Locate every blood parasite and identify its species.
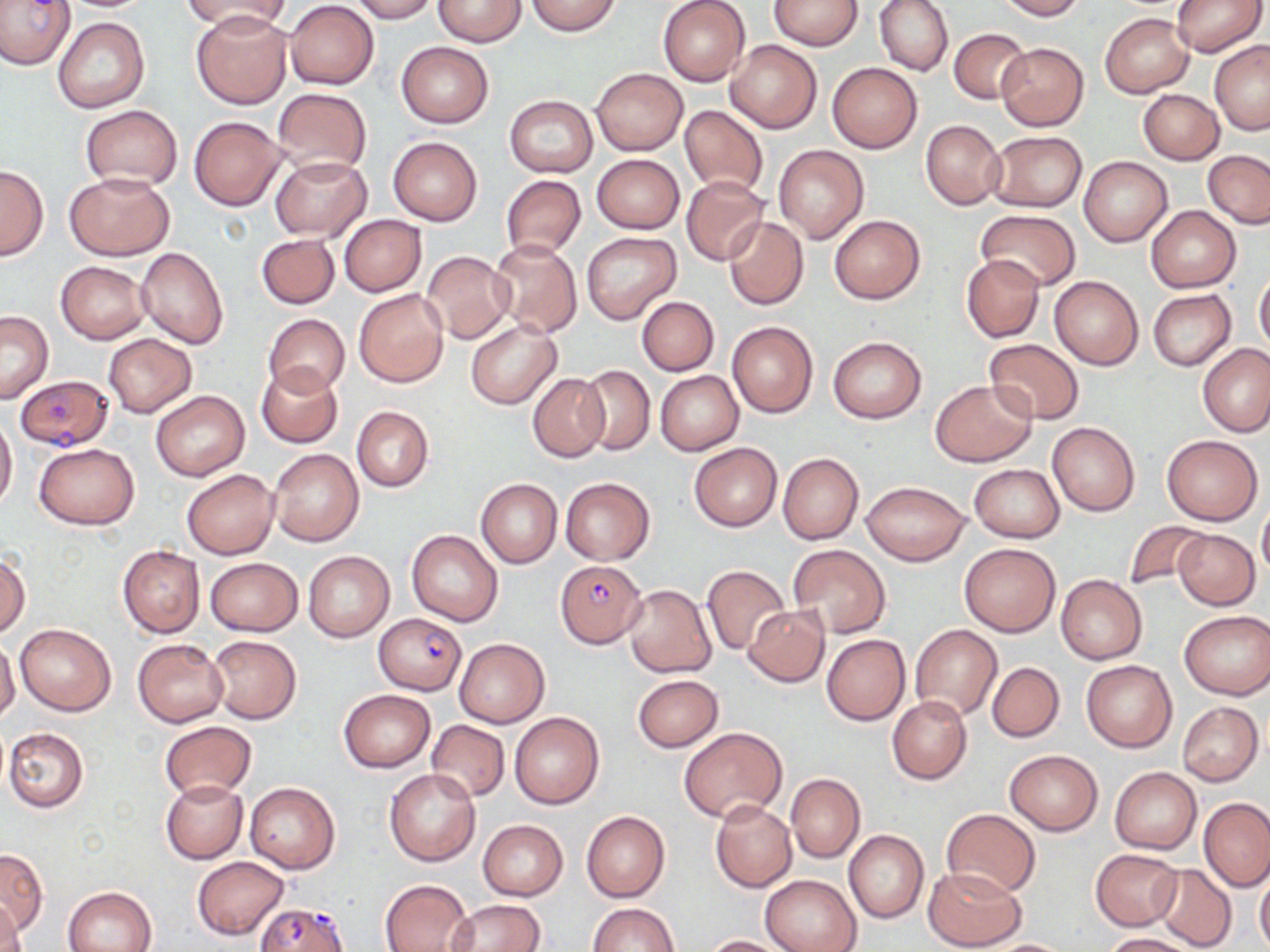
Approximate bounding boxes as [x1, y1, x2, y2] in pixels.
Plasmodium falciparum-infected red blood cells: [0, 0, 75, 69], [14, 375, 113, 450], [555, 559, 647, 647], [373, 612, 468, 694], [254, 902, 349, 952].
No Plasmodium ovale, Plasmodium malariae, Plasmodium vivax, Babesia divergens, or Trypanosoma brucei observed.

slide-level diagnosis = Plasmodium falciparum
field of view = single
modality = optical microscopy
magnification = 1000x
image size = 1270×952 pixels
stain = May-Grünwald-Giemsa
uninfected red blood cell locations = approximate bounding boxes as [x1, y1, x2, y2] in pixels: [348, 0, 436, 22], [433, 0, 527, 46], [658, 0, 750, 87], [768, 0, 863, 50], [874, 0, 953, 76], [996, 0, 1085, 20], [1169, 0, 1266, 58], [184, 1, 290, 35], [285, 1, 379, 89], [525, 1, 621, 36], [192, 12, 292, 109], [1101, 13, 1193, 98], [54, 17, 149, 114], [948, 28, 1030, 104], [725, 39, 820, 133], [1209, 41, 1270, 134], [396, 42, 493, 128], [996, 42, 1089, 130], [828, 62, 922, 153], [591, 68, 688, 155], [272, 86, 371, 178], [1138, 89, 1223, 164], [504, 94, 598, 176], [80, 105, 183, 190], [679, 105, 768, 197], [189, 115, 285, 210], [920, 119, 1006, 210], [987, 131, 1087, 213], [388, 136, 482, 225], [773, 145, 868, 243], [1203, 150, 1269, 228], [592, 153, 684, 235], [269, 156, 372, 241], [1079, 156, 1173, 247], [0, 164, 48, 261], [63, 171, 175, 261], [501, 176, 585, 259], [682, 177, 769, 265], [1147, 206, 1240, 293], [974, 211, 1080, 290], [339, 215, 426, 296], [830, 215, 925, 304], [723, 216, 809, 310], [580, 231, 681, 325], [256, 233, 340, 310], [487, 240, 583, 338], [136, 246, 230, 350], [421, 251, 515, 344], [961, 255, 1044, 342], [56, 262, 150, 345], [1254, 269, 1270, 354], [1050, 274, 1143, 370], [354, 289, 449, 387], [1148, 289, 1236, 371], [637, 296, 719, 376], [1, 311, 53, 402], [264, 313, 349, 397], [465, 318, 561, 409], [727, 320, 818, 418], [102, 333, 197, 417], [827, 336, 927, 423], [984, 339, 1084, 423], [1199, 343, 1269, 437], [256, 364, 342, 449], [574, 364, 655, 455], [529, 372, 610, 461], [655, 372, 743, 454], [930, 380, 1036, 467], [150, 390, 249, 481], [351, 405, 434, 491], [0, 413, 18, 509], [1047, 422, 1139, 516], [1161, 434, 1264, 526], [33, 442, 140, 530], [689, 442, 782, 532], [268, 448, 364, 547], [778, 452, 864, 544], [970, 464, 1063, 542], [181, 467, 279, 559], [561, 477, 654, 564], [476, 478, 562, 568], [860, 481, 970, 565], [1258, 503, 1270, 580], [1123, 520, 1212, 596], [406, 528, 503, 626], [1172, 529, 1259, 609], [960, 543, 1061, 636], [788, 544, 889, 638], [117, 545, 205, 637], [0, 550, 30, 638], [303, 551, 395, 643], [204, 558, 303, 636], [702, 564, 791, 656], [1055, 575, 1146, 665], [623, 584, 717, 678], [744, 605, 830, 686], [1179, 611, 1269, 699], [14, 622, 116, 716], [910, 624, 1001, 721], [208, 634, 301, 723], [821, 635, 910, 725], [132, 638, 228, 727], [454, 638, 549, 727], [0, 639, 20, 724], [1082, 659, 1177, 753], [987, 661, 1064, 742], [632, 674, 724, 752], [338, 689, 435, 773], [887, 695, 971, 784], [1178, 702, 1264, 785], [509, 712, 605, 809], [426, 720, 510, 801], [159, 721, 256, 800], [677, 726, 788, 822], [3, 727, 88, 813], [1004, 749, 1103, 835], [1110, 767, 1202, 854], [385, 769, 480, 866], [785, 773, 865, 862], [161, 779, 247, 864], [245, 782, 340, 874], [1200, 798, 1269, 891], [710, 800, 797, 892], [941, 809, 1041, 898], [581, 810, 670, 903], [478, 819, 567, 900], [844, 830, 928, 923], [0, 849, 47, 937], [1090, 849, 1182, 930], [192, 856, 290, 939], [1153, 863, 1235, 950], [923, 865, 1028, 951], [1255, 865, 1270, 951], [761, 875, 861, 952], [379, 879, 472, 952], [64, 886, 157, 952], [444, 900, 544, 951], [1, 901, 26, 952], [586, 903, 678, 952], [1100, 933, 1203, 952], [702, 935, 787, 951], [978, 939, 1077, 951]
preparation = thin blood smear